Mark where platelets are.
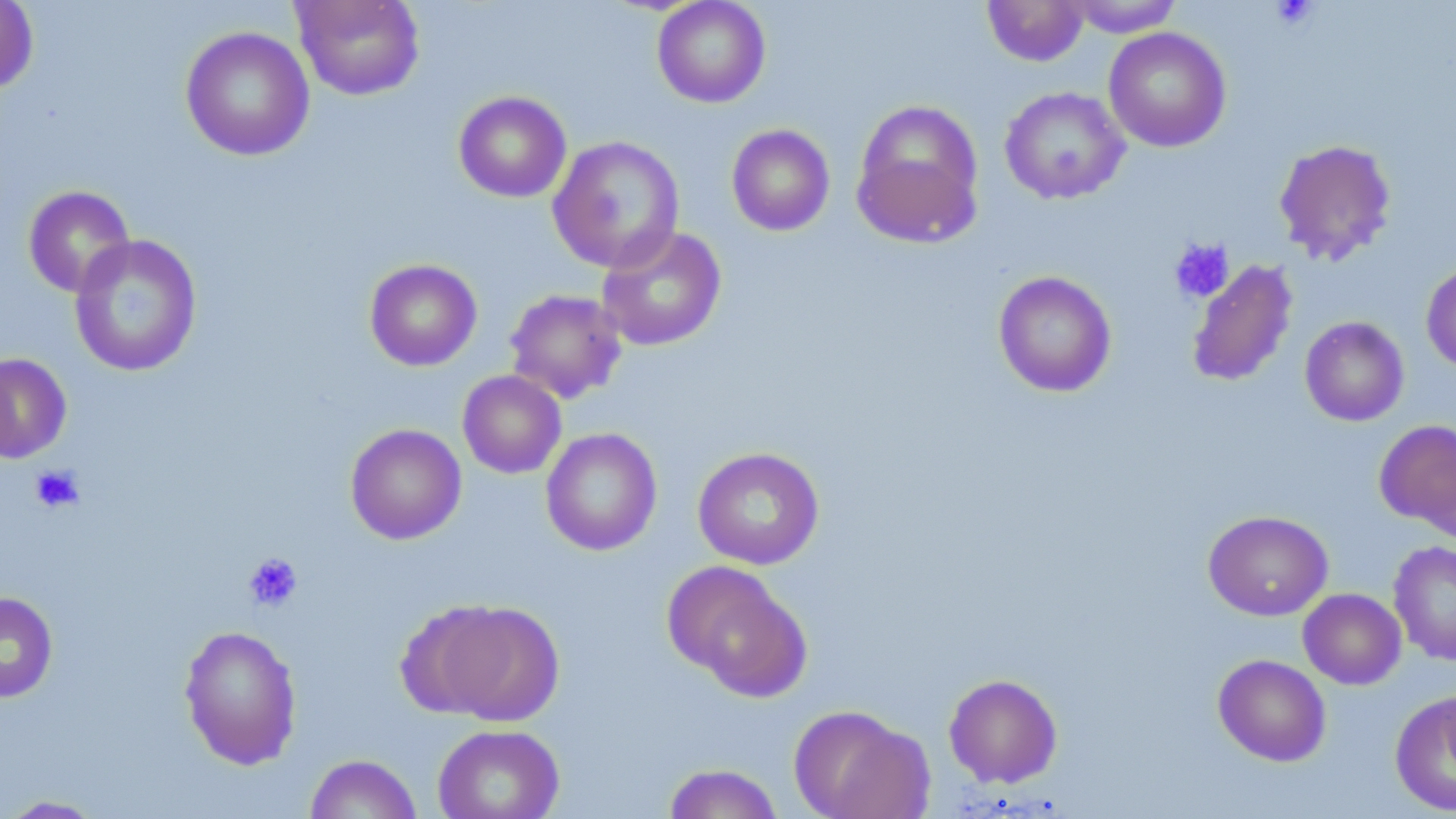

Approximate bounding boxes as (x1, y1, x2, y2) in pixels.
Platelets: (1269, 0, 1321, 32), (1169, 238, 1234, 303), (29, 464, 85, 514), (242, 552, 303, 612).

{
  "slide_level_diagnosis": "no evidence of blood parasites",
  "field_of_view": "single",
  "stain": "May-Grünwald-Giemsa",
  "modality": "light microscopy",
  "uninfected_red_blood_cell_locations": "approximate bounding boxes as (x1, y1, x2, y2) in pixels: (293, 0, 425, 101), (652, 0, 771, 108), (981, 0, 1090, 67), (1065, 0, 1185, 37), (0, 1, 38, 96), (180, 25, 315, 161), (1103, 27, 1231, 153), (999, 86, 1130, 204), (453, 91, 572, 203), (852, 101, 983, 245), (726, 124, 835, 236), (548, 135, 685, 273), (1273, 138, 1398, 266), (23, 185, 135, 298), (596, 224, 727, 352), (69, 234, 202, 377), (364, 258, 482, 371), (1186, 259, 1298, 388), (1421, 262, 1456, 374), (993, 270, 1117, 398), (504, 289, 627, 404), (1299, 316, 1410, 426), (1, 352, 72, 463), (457, 370, 567, 479), (1373, 420, 1456, 532), (345, 423, 467, 544), (541, 427, 663, 556), (692, 447, 825, 570), (1203, 510, 1334, 621), (1388, 540, 1456, 666), (664, 561, 813, 701), (1298, 588, 1407, 690), (0, 590, 58, 703), (435, 601, 565, 726), (179, 624, 302, 770), (1213, 654, 1331, 767), (943, 673, 1063, 788), (1389, 690, 1456, 816), (788, 704, 932, 818), (432, 723, 564, 819), (304, 753, 422, 818), (661, 763, 784, 819), (1, 795, 108, 818)",
  "preparation": "thin blood film",
  "magnification": "1000x",
  "image_size": "1456×819 pixels"
}